Name the cell type shown.
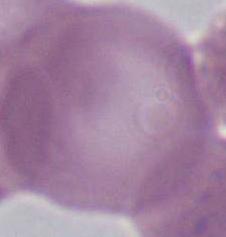

An erythrocyte.

Summary:
  - Magnification: 1000x
  - Modality: micrograph